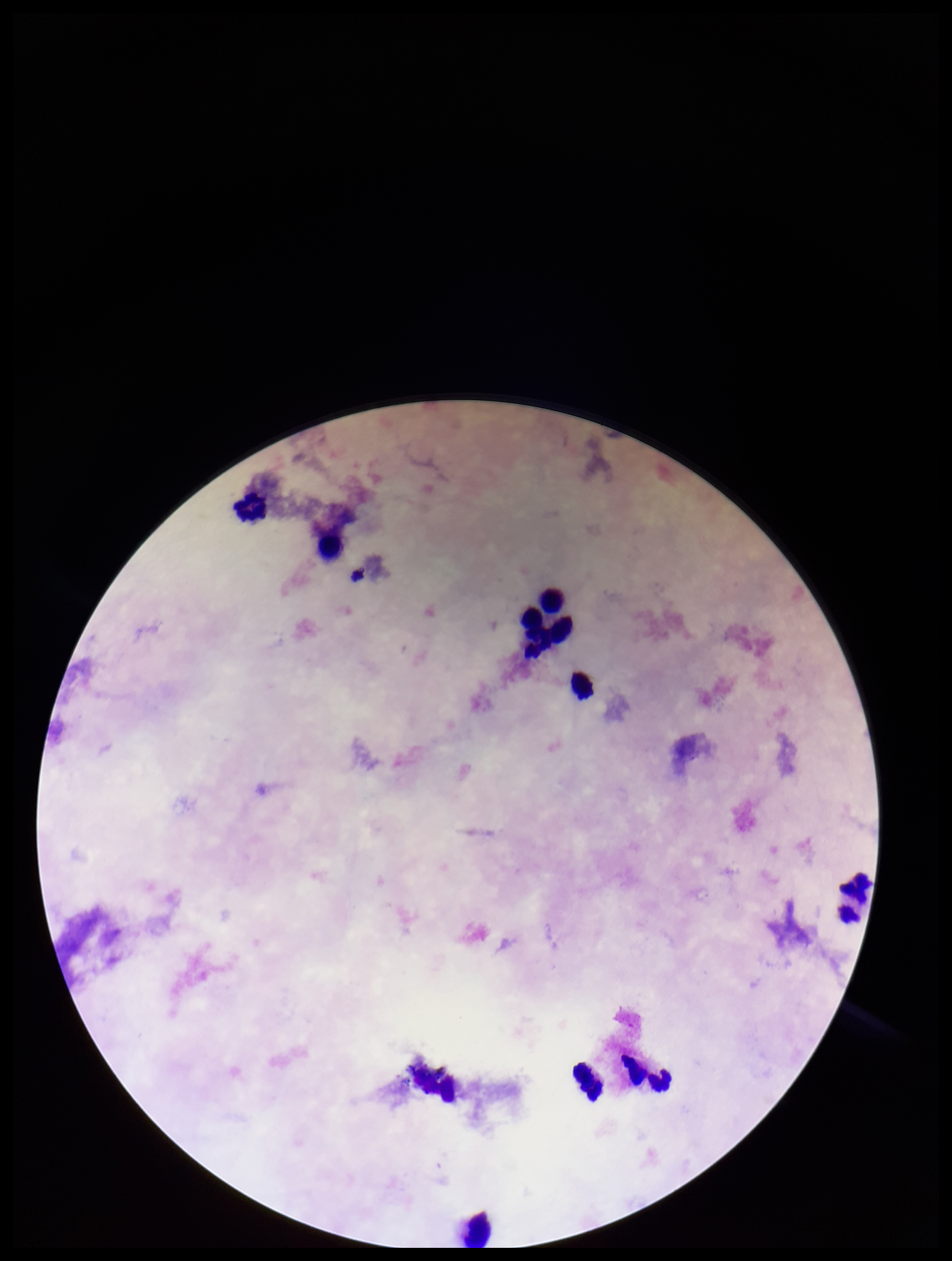 Parasite count: 0. Image is 952×1261 pixels. Leukocyte count: 9. Stained with Giemsa. Patient malaria status: negative. One field from this slide. Preparation: thick smear. Smartphone photograph taken through the eyepiece of a microscope. Plasmodium parasites: none seen.